Name the parasite shown.
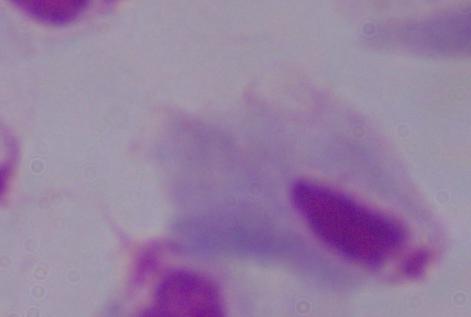
This is a trichomonad.

Summary:
  - Modality: micrograph
  - Magnification: 1000x